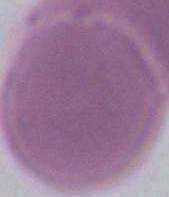
magnification = 1000x
modality = photomicrograph
identification = red blood cell